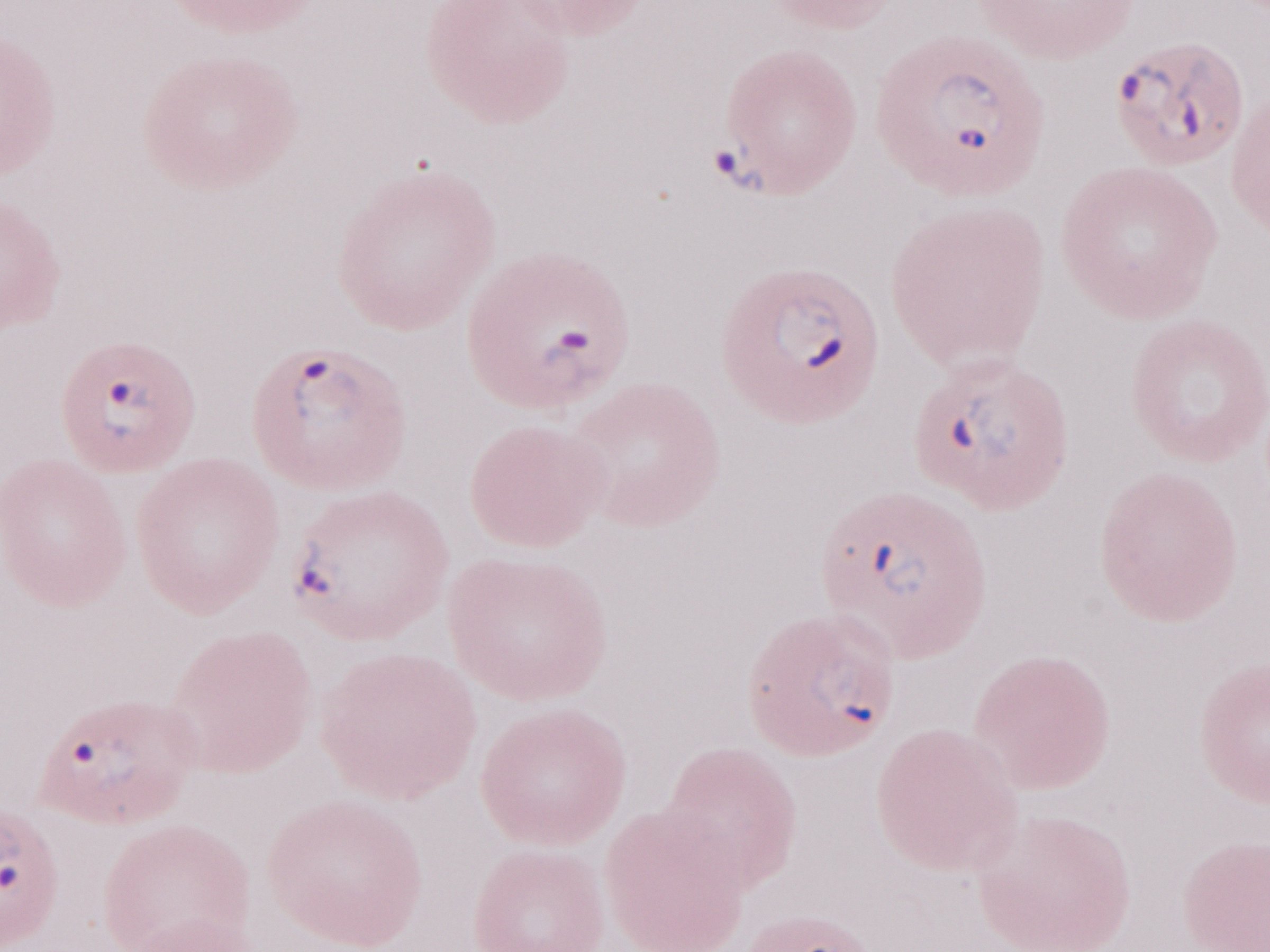 Thin peripheral-blood smear. Olympus BX43 microscope, Olympus DP73 camera. One field of this slide. Malaria diagnosis (patient-level): positive. May-Grünwald-Giemsa (MGG) stain. Image is 1270×952 pixels. Magnification: 1,000x.